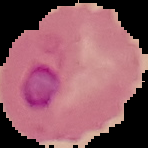
{
  "image_type": "segmented cell region on a black background",
  "result": "malaria parasites identified",
  "preparation": "thin blood smear",
  "image_size": "148×148 pixels"
}